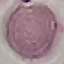

Malaria status: uninfected. Automatically extracted cell patch, resized to 64 × 64 pixels. Thin smear of blood. Acquired by smartphone through the microscope eyepiece. Giemsa-stained preparation.